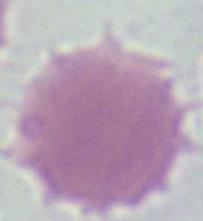

modality = photomicrograph
identification = red blood cell
magnification = 1000x